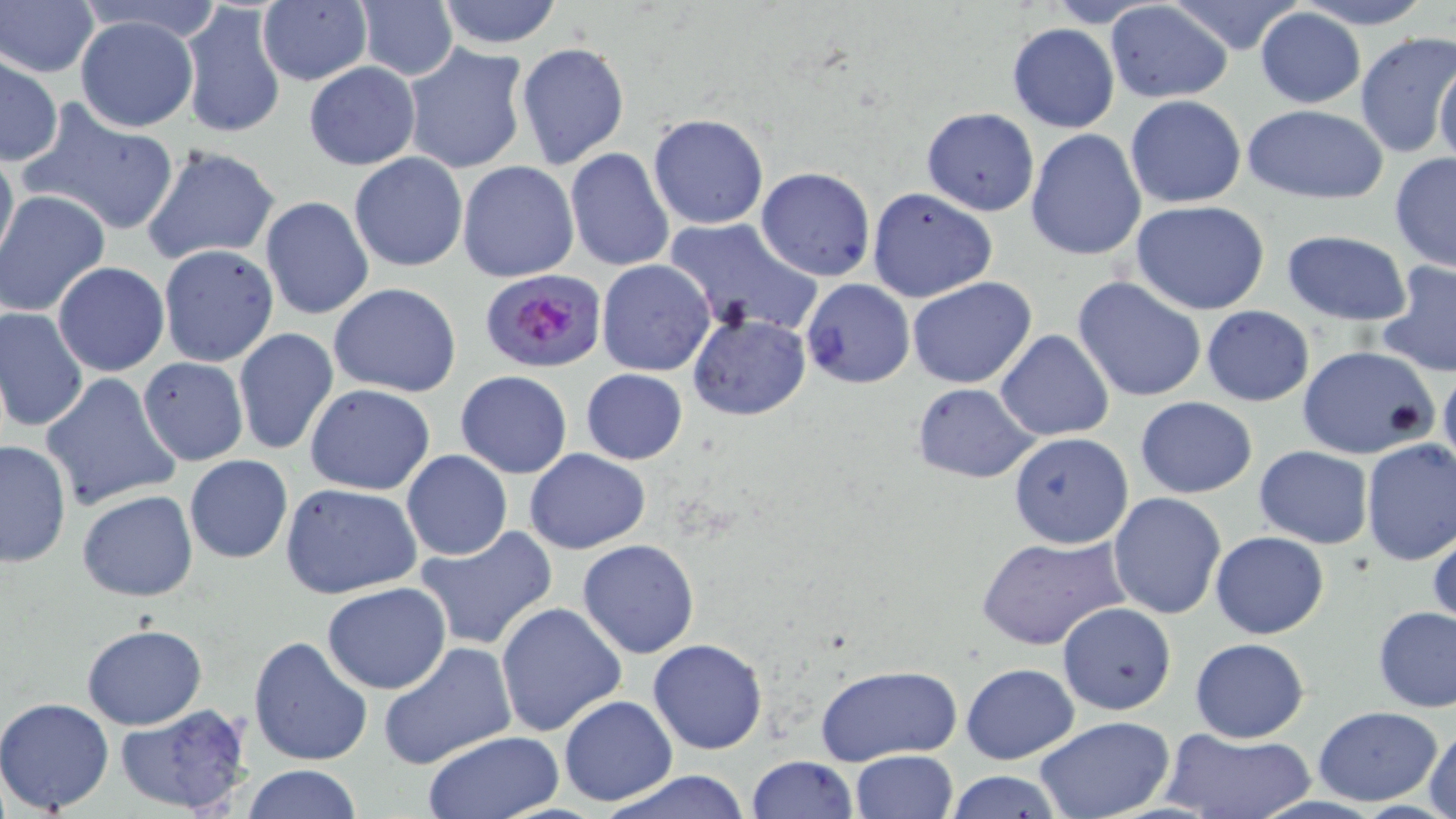
Summary:
  - Coordinate format: approximate bounding boxes as (x1, y1, x2, y2) in pixels
  - Uninfected red blood cell locations: (434, 0, 565, 48), (1288, 0, 1443, 29), (355, 1, 458, 81), (1104, 1, 1235, 104), (1, 2, 98, 77), (179, 2, 286, 142), (258, 3, 371, 86), (1254, 8, 1366, 108), (73, 15, 200, 132), (1008, 23, 1120, 133), (1355, 32, 1454, 159), (515, 41, 629, 170), (403, 43, 530, 175), (2, 54, 63, 164), (1434, 57, 1456, 170), (304, 62, 419, 170), (1124, 95, 1246, 209), (26, 101, 180, 232), (1241, 103, 1389, 205), (921, 107, 1039, 215), (899, 110, 1025, 296), (648, 112, 769, 230), (1025, 129, 1148, 262), (141, 144, 279, 265), (565, 147, 674, 272), (0, 149, 18, 268), (349, 152, 468, 272), (1389, 154, 1456, 272), (458, 161, 578, 282), (756, 168, 875, 280), (868, 187, 997, 303), (0, 190, 113, 319), (261, 196, 374, 320), (1130, 201, 1273, 316), (660, 217, 822, 336), (1281, 230, 1414, 326), (158, 245, 279, 368), (597, 259, 715, 377), (1376, 261, 1456, 380), (53, 262, 169, 377), (1071, 275, 1209, 404), (907, 276, 1036, 388), (799, 278, 916, 389), (329, 283, 462, 397), (1201, 305, 1314, 406), (1, 306, 89, 433), (687, 313, 810, 421), (233, 328, 338, 456), (993, 331, 1113, 441), (1298, 347, 1439, 460), (136, 356, 249, 465), (1438, 367, 1456, 478), (581, 368, 688, 465), (455, 370, 572, 478), (40, 372, 181, 512), (910, 382, 1039, 483), (305, 384, 435, 495), (1135, 396, 1258, 498), (1008, 431, 1132, 549), (1360, 439, 1456, 568), (0, 440, 72, 567), (1254, 445, 1374, 548), (525, 448, 651, 553), (401, 449, 512, 562), (184, 455, 293, 563), (280, 483, 424, 600), (78, 490, 198, 602), (1107, 491, 1227, 619), (1428, 523, 1456, 632), (414, 525, 557, 651), (1210, 531, 1328, 639), (977, 534, 1131, 649), (577, 539, 701, 658), (321, 583, 451, 694), (495, 602, 626, 738), (1057, 602, 1177, 715), (1374, 607, 1456, 712), (81, 625, 207, 730), (247, 635, 372, 766), (1188, 636, 1309, 742), (648, 639, 767, 754), (376, 641, 518, 771), (960, 663, 1080, 764), (815, 664, 961, 767), (0, 696, 115, 815), (557, 696, 678, 807), (115, 702, 252, 816), (1314, 706, 1442, 805), (1034, 716, 1174, 819), (1425, 723, 1456, 819), (1162, 727, 1316, 818), (422, 731, 563, 817), (850, 749, 958, 818), (746, 755, 858, 818), (242, 764, 362, 819), (596, 769, 757, 819), (943, 770, 1066, 818)
  - Plasmodium falciparum-infected red blood cell locations: (479, 269, 607, 374)
  - Slide-level diagnosis: Plasmodium falciparum
  - Preparation: thin blood film
  - Field of view: single
  - Magnification: 1000x
  - Image size: 1456×819 pixels
  - Modality: optical microscopy
  - Stain: May-Grünwald-Giemsa